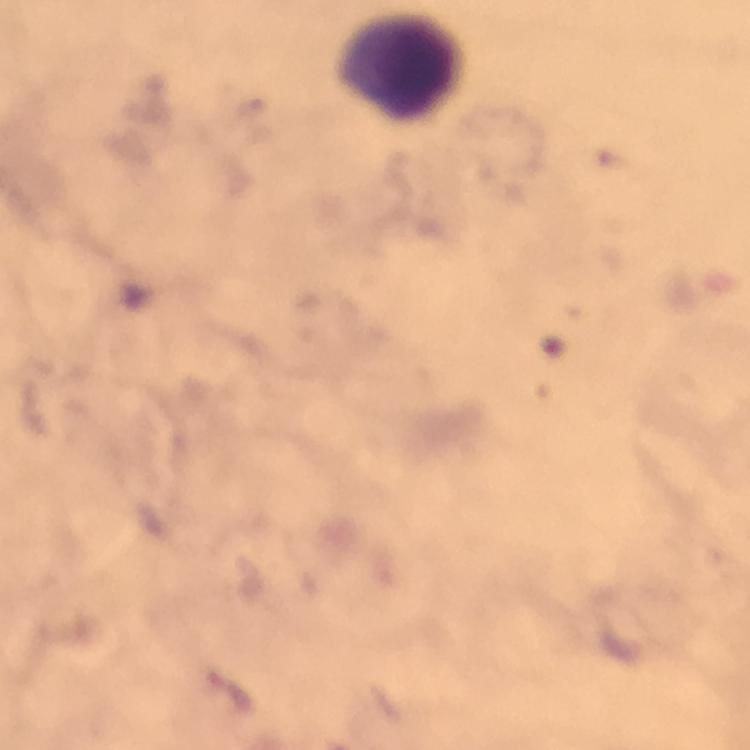
context = from a diagnostic examination for malaria
cropped from = one field of view
image size = 750×750 pixels
immersion oil = used
magnification = 100x
preparation = thick blood film
Plasmodium parasites = none detected
stain = Giemsa
leukocyte locations = approximate object centers, in pixels from the top-left corner: (x=404, y=65)
capture = smartphone camera through the microscope